Assess this cell for malaria.
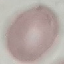
Uninfected.

Giemsa-stained preparation. Automatically extracted cell patch, resized to 64 × 64 pixels. Photographed with a smartphone camera at the microscope eyepiece. Thin blood smear.